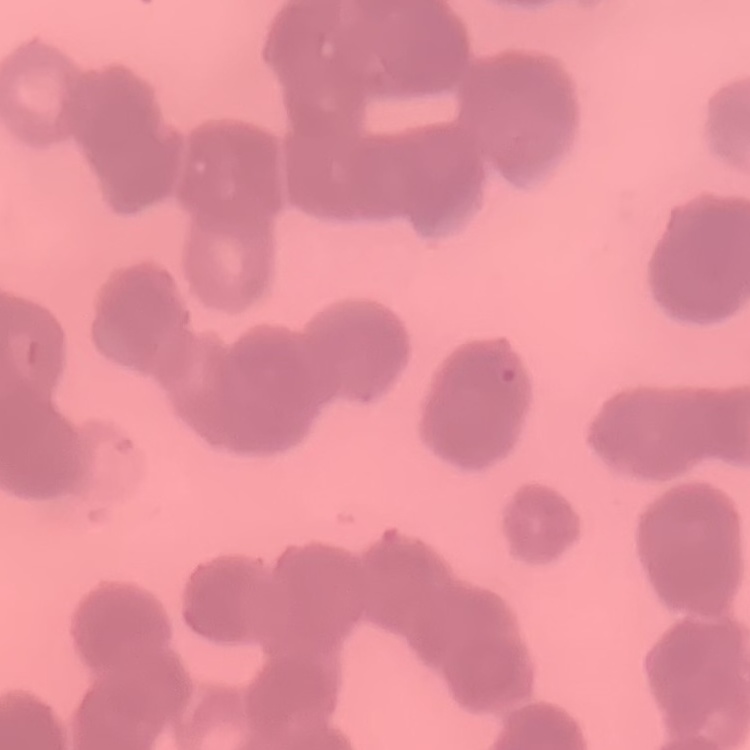
The red blood cells show rouleaux formation. Thin blood smear. Field's or Giemsa stain. Square crop of a larger photomicrograph.